Identify the cell.
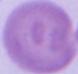

An erythrocyte.

1000x magnification. Micrograph.